State which cell type is depicted.
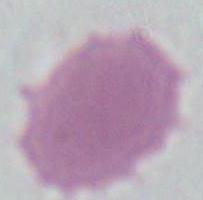

This is an erythrocyte.

Summary:
  - Magnification: 1000x
  - Modality: micrograph